State which parasite is depicted.
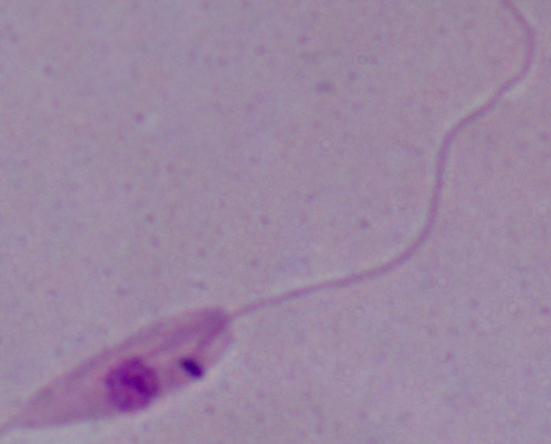

Leishmania.

Summary:
  - Magnification: 1000x
  - Modality: photomicrograph